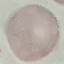

Result: no malaria parasites detected. Giemsa-stained preparation. Cell patch, automatically extracted from a larger field of view and resized to 64 × 64 pixels. Photographed with a smartphone camera at the microscope eyepiece. Thin blood film.